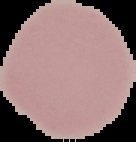
{
  "malaria_status": "uninfected",
  "preparation": "thin blood film",
  "image_size": "136×142 pixels",
  "image_type": "cell region segmented out of the field of view; surrounding area masked to black"
}